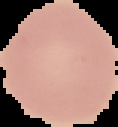
From a thin blood smear. Result: no malaria parasites detected. Image is 118×127 pixels. The area outside the segmented cell region is set to black.